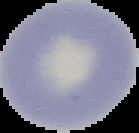
image_size: 139×133 pixels
preparation: thin blood film
result: no Plasmodium parasites detected
image_type: cell region segmented out of the field of view; surrounding area masked to black